Assess this cell for malaria.
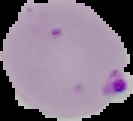
It is parasitized.

From a thin blood smear. Image is 133×121 pixels. Cell region segmented out of the field of view; the surrounding area is masked to black.